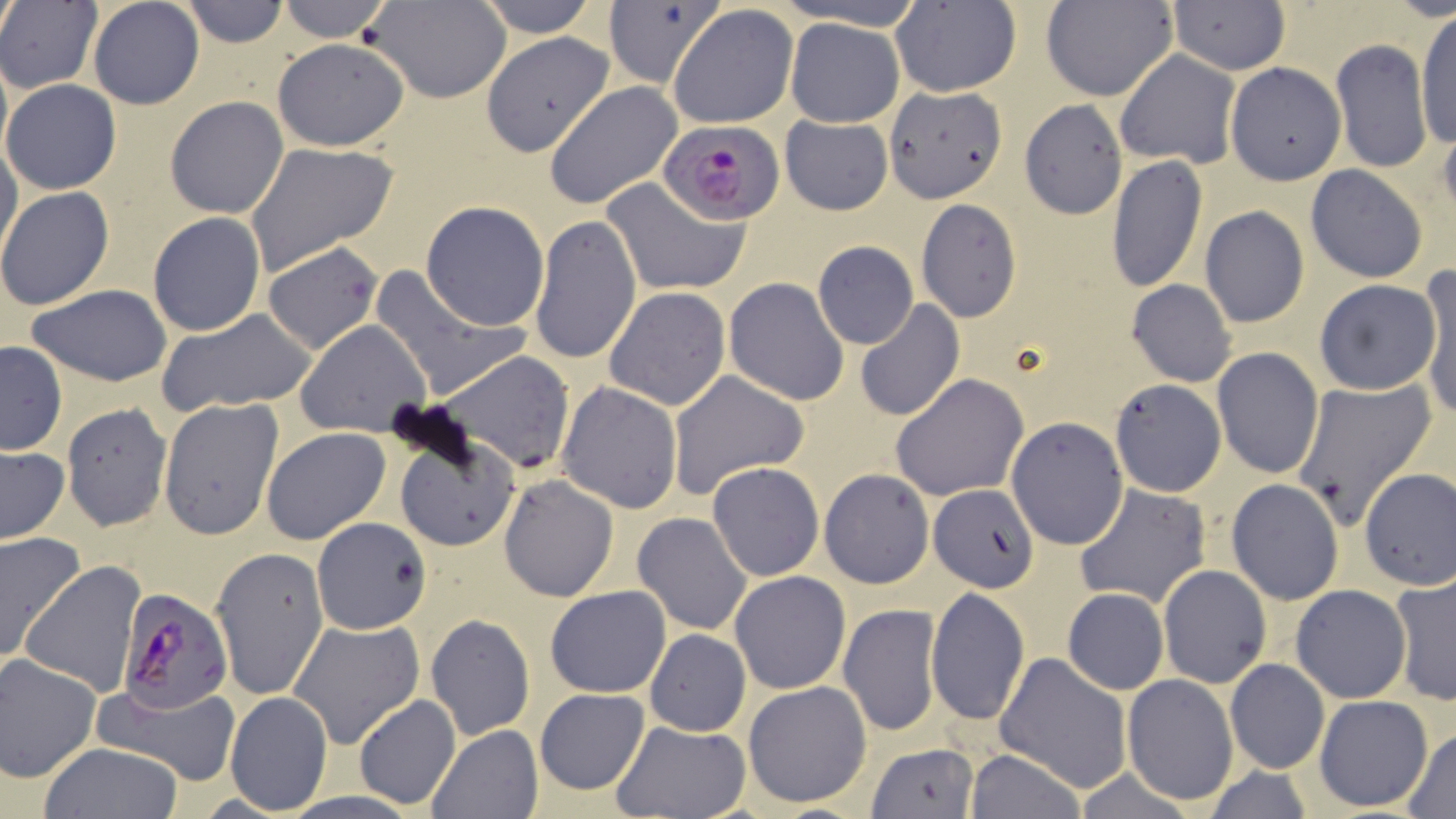
slide_level_diagnosis: Plasmodium falciparum
modality: optical microscopy
stain: May-Grünwald-Giemsa
plasmodium_falciparum_infected_red_blood_cell_locations: 'approximate bounding boxes as (x1, y1, x2, y2) in pixels: (661, 119, 788, 227), (121, 589, 238, 718)'
field_of_view: single
image_size: 1456×819 pixels
preparation: thin blood smear
magnification: 1000x
uninfected_red_blood_cell_locations: 'approximate bounding boxes as (x1, y1, x2, y2) in pixels: (87, 0, 204, 110), (180, 0, 286, 47), (364, 0, 511, 104), (474, 0, 602, 36), (776, 0, 928, 30), (1043, 0, 1179, 101), (0, 1, 101, 92), (274, 1, 394, 42), (602, 1, 722, 90), (892, 1, 1020, 97), (1167, 2, 1290, 75), (669, 3, 799, 129), (1415, 10, 1455, 154), (784, 17, 904, 126), (481, 33, 615, 158), (272, 38, 410, 152), (1331, 39, 1432, 173), (1114, 50, 1241, 169), (1223, 61, 1346, 186), (1, 78, 122, 196), (544, 82, 682, 209), (885, 85, 1007, 204), (165, 96, 289, 219), (1020, 101, 1130, 220), (780, 114, 893, 215), (0, 140, 22, 266), (245, 141, 400, 275), (1106, 155, 1207, 293), (1306, 166, 1429, 281), (602, 177, 749, 297), (0, 187, 114, 311), (915, 199, 1022, 322), (421, 200, 549, 330), (1200, 205, 1309, 328), (148, 212, 266, 336), (529, 214, 642, 364), (263, 241, 383, 354), (812, 242, 918, 349), (368, 266, 524, 402), (1416, 266, 1456, 416), (724, 277, 849, 405), (1312, 278, 1442, 395), (1125, 279, 1237, 386), (27, 285, 173, 385), (603, 287, 731, 411), (856, 299, 964, 421), (157, 307, 318, 415), (295, 319, 433, 438), (0, 341, 67, 455), (1211, 347, 1325, 478), (433, 350, 575, 476), (666, 370, 811, 499), (891, 374, 1028, 501), (1290, 377, 1439, 531), (1110, 378, 1227, 498), (556, 381, 682, 513), (158, 397, 284, 540), (61, 402, 171, 531), (1006, 416, 1127, 549), (261, 426, 392, 546), (393, 429, 524, 554), (0, 447, 70, 544), (707, 462, 823, 581), (714, 465, 836, 695), (1357, 466, 1456, 593), (819, 468, 934, 589), (498, 474, 618, 602), (1225, 479, 1343, 605), (929, 484, 1039, 593), (1074, 484, 1211, 610), (631, 512, 753, 636), (311, 518, 431, 636), (0, 532, 86, 664), (210, 545, 328, 700), (19, 559, 147, 698), (1159, 565, 1271, 687), (730, 571, 850, 694), (1390, 571, 1455, 706), (1290, 583, 1412, 705), (545, 584, 670, 698), (927, 587, 1029, 723), (1061, 588, 1167, 695), (838, 602, 941, 736), (425, 614, 535, 741), (287, 618, 424, 749), (643, 628, 752, 737), (994, 651, 1132, 791), (0, 654, 101, 782), (1225, 658, 1329, 775), (1220, 672, 1410, 794), (1122, 674, 1238, 806), (742, 680, 873, 811), (92, 684, 242, 783), (533, 687, 651, 795), (225, 692, 333, 815), (354, 695, 459, 811), (1314, 695, 1434, 810), (613, 720, 751, 817), (428, 725, 542, 818), (1402, 729, 1455, 816), (38, 742, 183, 819), (864, 742, 979, 819), (965, 749, 1088, 819)'